Assess the morphology of the red blood cells.
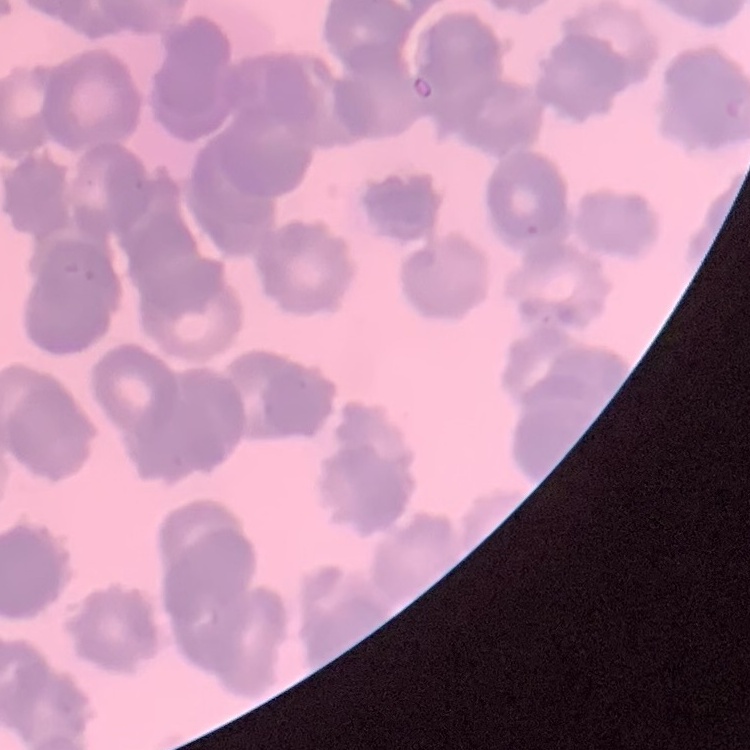
They show rouleaux formation.

Summary:
  - Preparation: thin peripheral smear
  - Image type: square crop of a larger photomicrograph
  - Stain: Field's or Giemsa